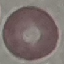

result = no malaria parasites detected
stain = Giemsa
image type = cell patch, automatically extracted from a larger field of view and resized to 64 × 64 pixels
capture = smartphone camera at the microscope eyepiece
preparation = thin blood smear